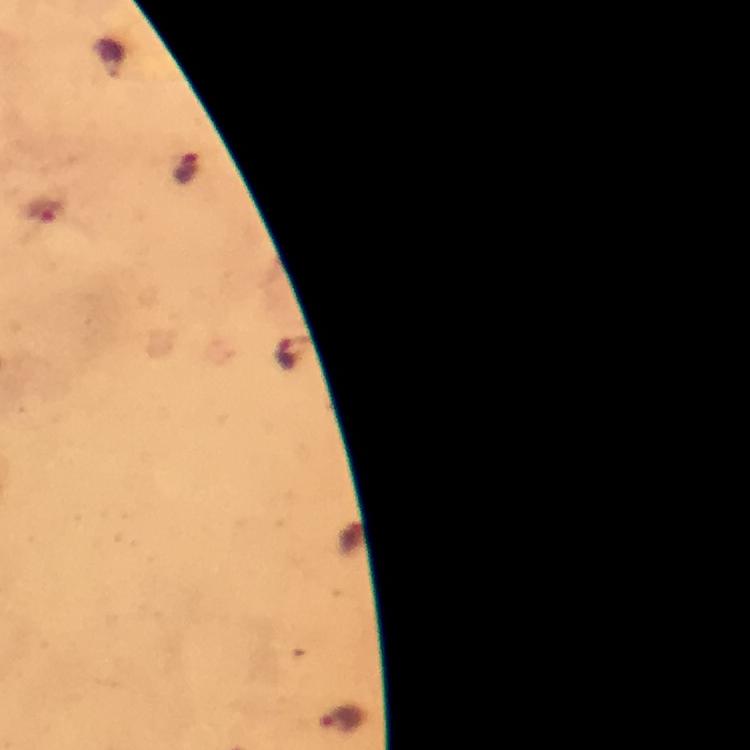 Approximate centers as {x, y} in pixels. Malaria parasite locations: {289, 354}. Immersion oil applied. Image is 750×750 pixels. Thick smear. Giemsa-stained preparation. From a diagnostic examination for malaria. Photographed through the microscope with a smartphone camera. 100x magnification. Cropped region of a single field of view.